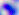 Toxoplasma gondii is shown. 400x magnification. Micrograph.